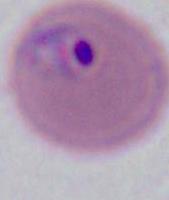

Summary:
  - Modality: photomicrograph
  - Magnification: 400x or 1000x
  - Identification: Plasmodium